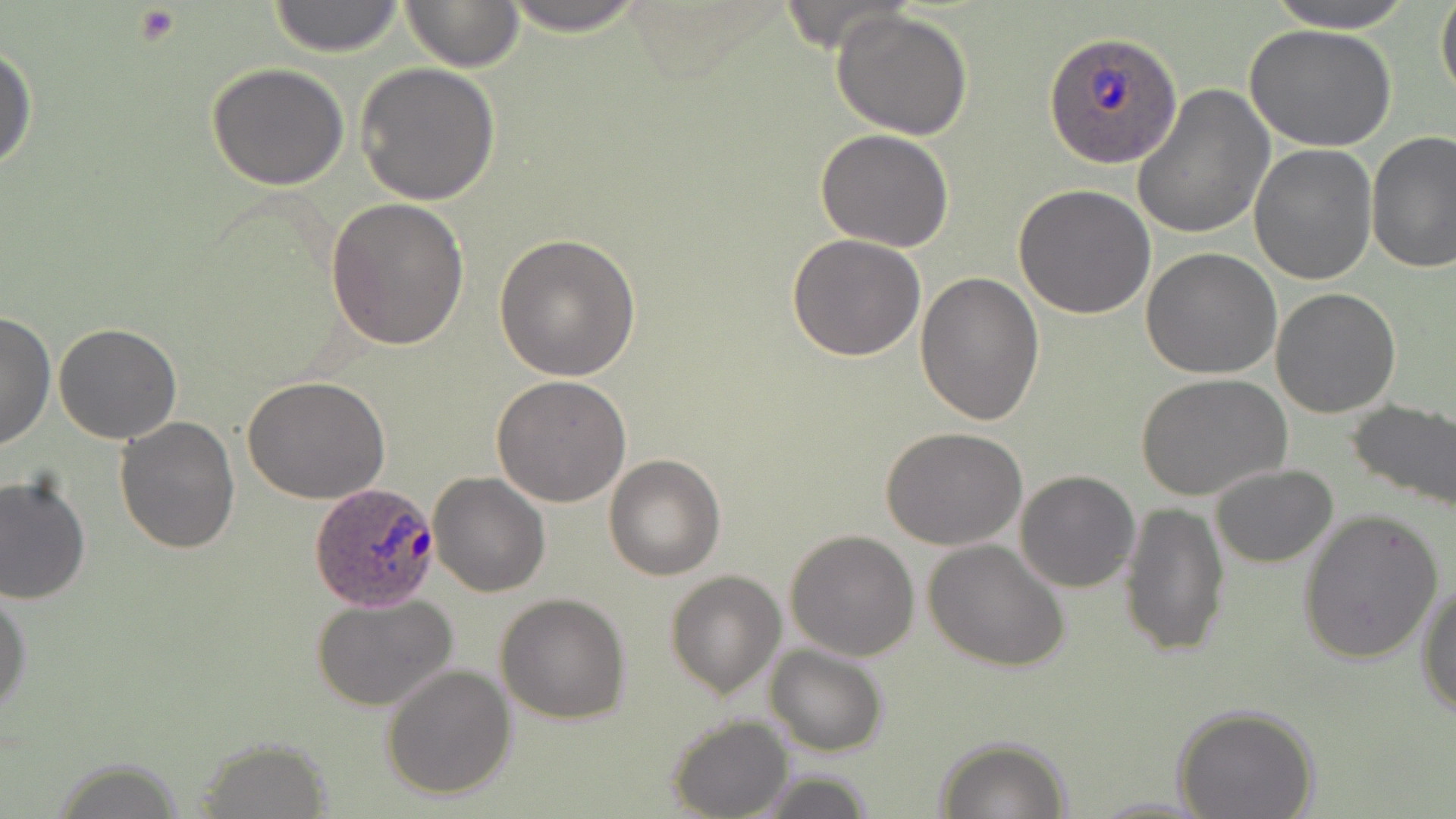
Approximate bounding boxes as named x1/y1/x2/y2 corners in pixels. Plasmodium ovale-infected red blood cell locations: (x1=1044, y1=32, x2=1183, y2=170), (x1=309, y1=481, x2=441, y2=610). Platelet locations: (x1=132, y1=5, x2=183, y2=45). Uninfected red blood cell locations: (x1=264, y1=0, x2=408, y2=56), (x1=398, y1=0, x2=526, y2=71), (x1=490, y1=0, x2=655, y2=35), (x1=1257, y1=0, x2=1422, y2=32), (x1=1436, y1=0, x2=1456, y2=107), (x1=830, y1=8, x2=975, y2=140), (x1=1245, y1=24, x2=1396, y2=152), (x1=0, y1=43, x2=37, y2=177), (x1=356, y1=61, x2=500, y2=204), (x1=206, y1=63, x2=351, y2=189), (x1=1131, y1=85, x2=1274, y2=241), (x1=814, y1=128, x2=955, y2=252), (x1=1366, y1=131, x2=1456, y2=273), (x1=1249, y1=145, x2=1379, y2=285), (x1=1013, y1=184, x2=1156, y2=320), (x1=327, y1=197, x2=469, y2=348), (x1=495, y1=233, x2=641, y2=381), (x1=785, y1=234, x2=926, y2=361), (x1=1141, y1=248, x2=1282, y2=378), (x1=913, y1=269, x2=1043, y2=425), (x1=1270, y1=287, x2=1402, y2=418), (x1=0, y1=310, x2=54, y2=452), (x1=52, y1=323, x2=183, y2=444), (x1=492, y1=374, x2=632, y2=506), (x1=1137, y1=374, x2=1292, y2=504), (x1=243, y1=376, x2=390, y2=504), (x1=1345, y1=397, x2=1456, y2=514), (x1=113, y1=417, x2=241, y2=556), (x1=882, y1=426, x2=1028, y2=550), (x1=603, y1=454, x2=727, y2=580), (x1=1209, y1=463, x2=1337, y2=568), (x1=1015, y1=470, x2=1141, y2=593), (x1=428, y1=472, x2=550, y2=597), (x1=1, y1=473, x2=91, y2=607), (x1=1119, y1=500, x2=1230, y2=658), (x1=1296, y1=508, x2=1444, y2=662), (x1=785, y1=529, x2=920, y2=661), (x1=922, y1=539, x2=1069, y2=671), (x1=665, y1=569, x2=787, y2=698), (x1=1417, y1=581, x2=1456, y2=719), (x1=0, y1=587, x2=33, y2=722), (x1=311, y1=592, x2=459, y2=714), (x1=495, y1=593, x2=632, y2=723), (x1=764, y1=644, x2=888, y2=757), (x1=380, y1=662, x2=516, y2=800), (x1=1171, y1=702, x2=1320, y2=819), (x1=666, y1=715, x2=793, y2=819), (x1=934, y1=736, x2=1071, y2=818), (x1=193, y1=742, x2=333, y2=815), (x1=48, y1=759, x2=192, y2=818), (x1=750, y1=770, x2=877, y2=819). Slide-level diagnosis: Plasmodium ovale. Thin blood film. May-Grünwald-Giemsa-stained preparation. Light microscopy. 1000x magnification. One field of a larger specimen. Image is 1456×819 pixels.